Point out each leukocyte.
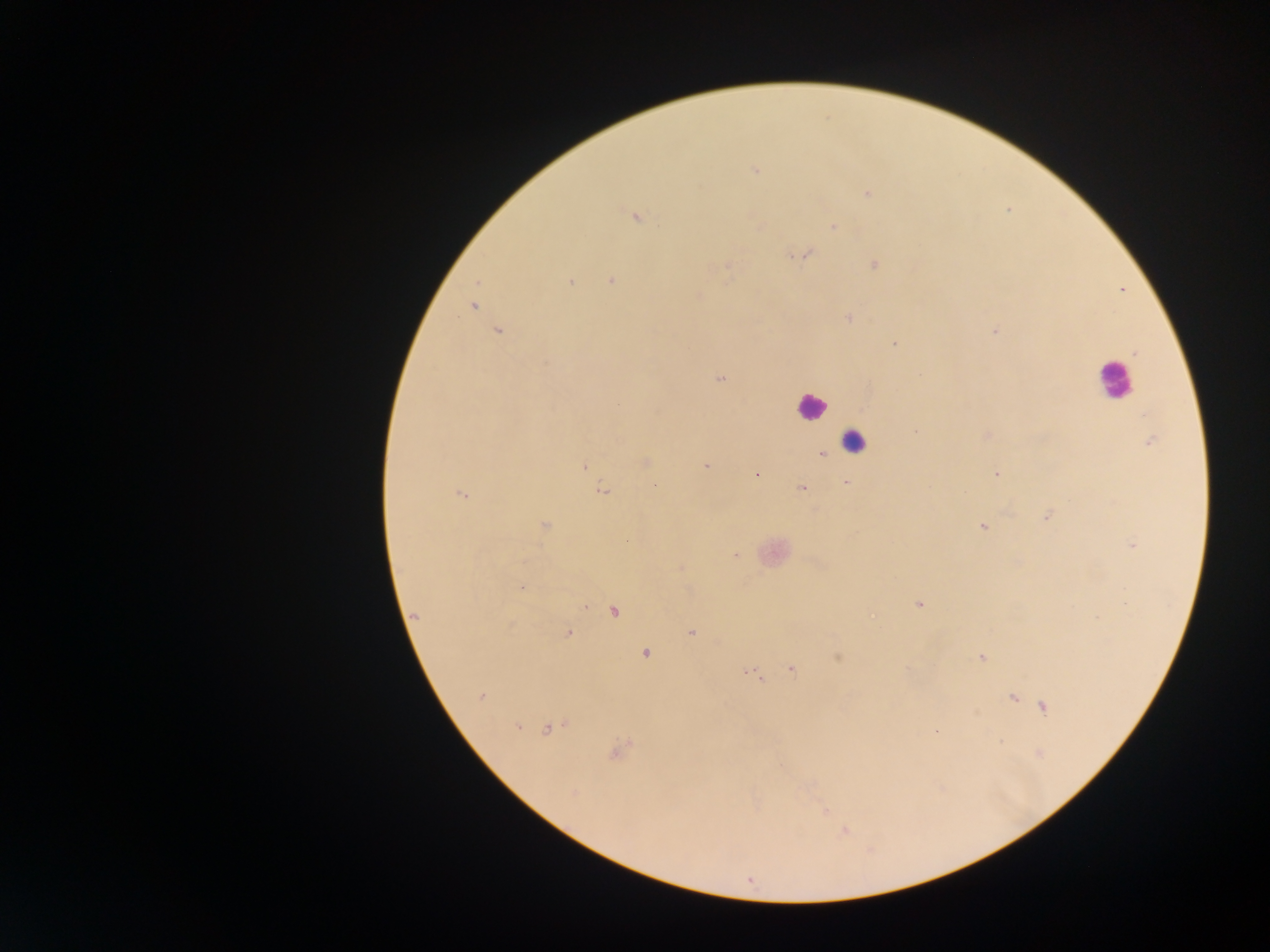

Approximate centers as x y in pixels.
Leukocytes: 1115 381; 811 406; 853 441.

Malaria parasite locations: 755 170; 867 193; 635 217; 833 226; 803 254; 875 264; 727 265; 611 280; 570 282; 700 296; 472 306; 848 319; 996 331; 498 332; 894 343; 1135 353; 720 379; 1144 414; 917 430; 987 435; 1150 443; 821 454; 646 461; 584 466; 705 466; 996 474; 755 475; 846 482; 655 485; 802 488; 602 492; 461 494; 1047 517; 544 526; 983 527; 1133 545; 736 555; 522 587; 919 604; 584 607; 614 611; 415 616; 691 633; 568 634; 646 654; 837 658; 981 658; 791 669; 752 673; 481 697; 1012 698; 1044 707; 517 727; 547 729; 936 731; 618 752; 574 794; 826 812; 845 832. Sample from Ghana. Single field of view. Thick blood film. Photographed through a microscope with a mobile-phone camera. Image is 1270×952 pixels.